Classify this cell by malaria status.
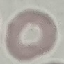
It is uninfected.

Summary:
  - Capture: smartphone through the microscope eyepiece
  - Stain: Giemsa
  - Image type: cell patch, automatically extracted from a larger field of view and resized to 64 × 64 pixels
  - Preparation: thin blood film